Report the malaria status of this cell.
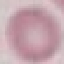
It is uninfected.

image_type: cell patch, automatically extracted from a larger field of view and resized to 64 × 64 pixels
capture: smartphone through the microscope eyepiece
preparation: thin blood smear
stain: Giemsa